Report the malaria status of this cell.
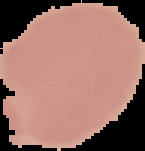
It is uninfected.

From a thin blood film. Image is 145×151 pixels. The area outside the segmented cell region is set to black.